Classify this cell by malaria status.
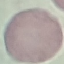
It is uninfected.

stain = Giemsa
preparation = thin blood smear
image type = automatically extracted cell patch, resized to 64 × 64 pixels
capture = smartphone through the microscope eyepiece